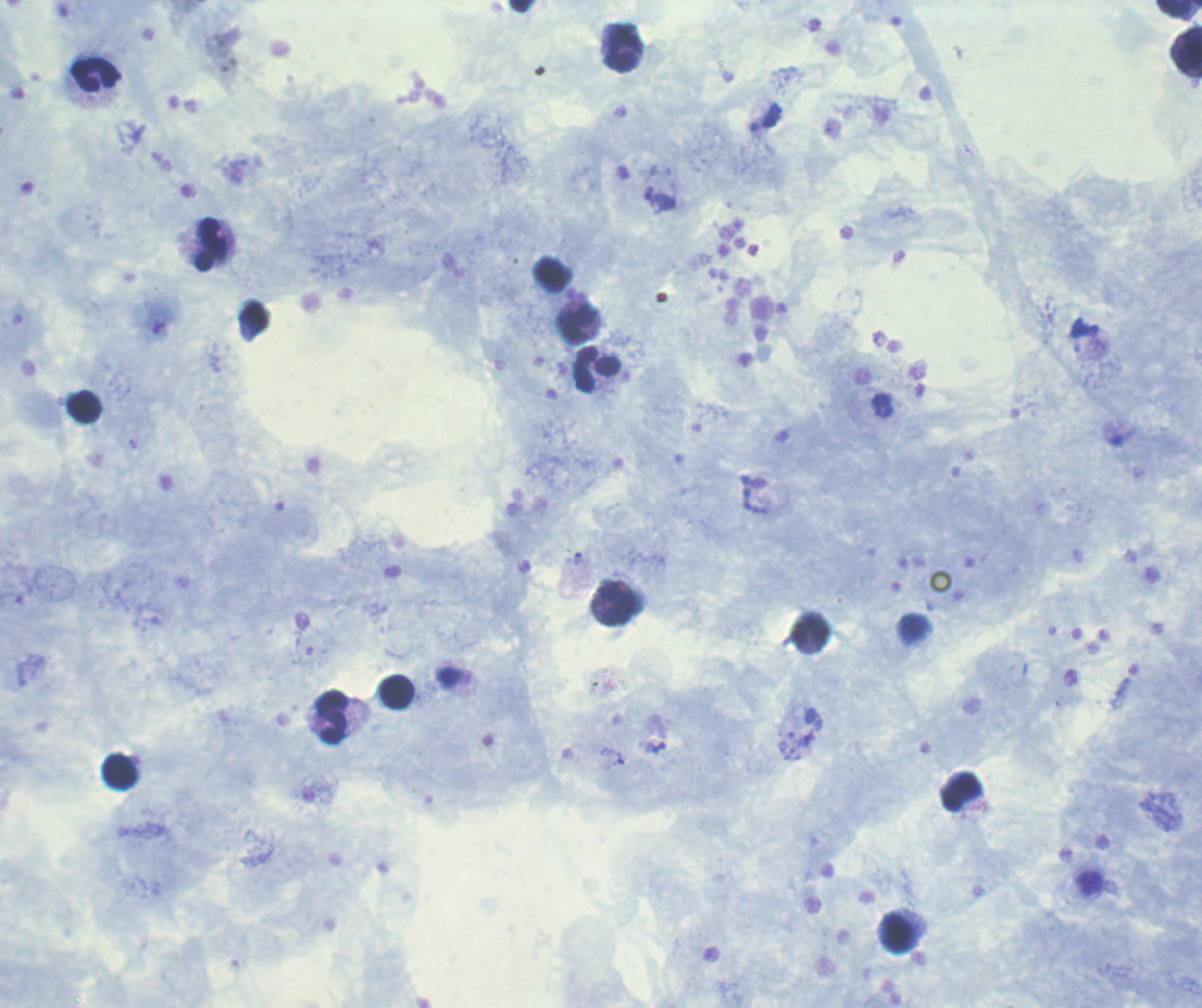
coordinate format = approximate centers as (x, y) in pixels
leukocyte locations = (1179, 10), (623, 48), (1186, 52), (95, 74), (210, 244), (255, 318), (578, 325), (597, 369), (84, 406), (617, 605), (812, 632), (397, 691), (332, 718), (120, 772), (961, 792), (899, 933)
trophozoite locations = (660, 201), (1085, 328), (578, 559), (613, 757)
stain = Romanowsky
image size = 1202×1008 pixels
field of view = single
coloration quality = good
result = positive for Plasmodium parasites
context = previously used in a real diagnosis
background quality = satisfactory
magnification = 100x
preparation = thick smear of blood